Locate every leukocyte (white blood cell).
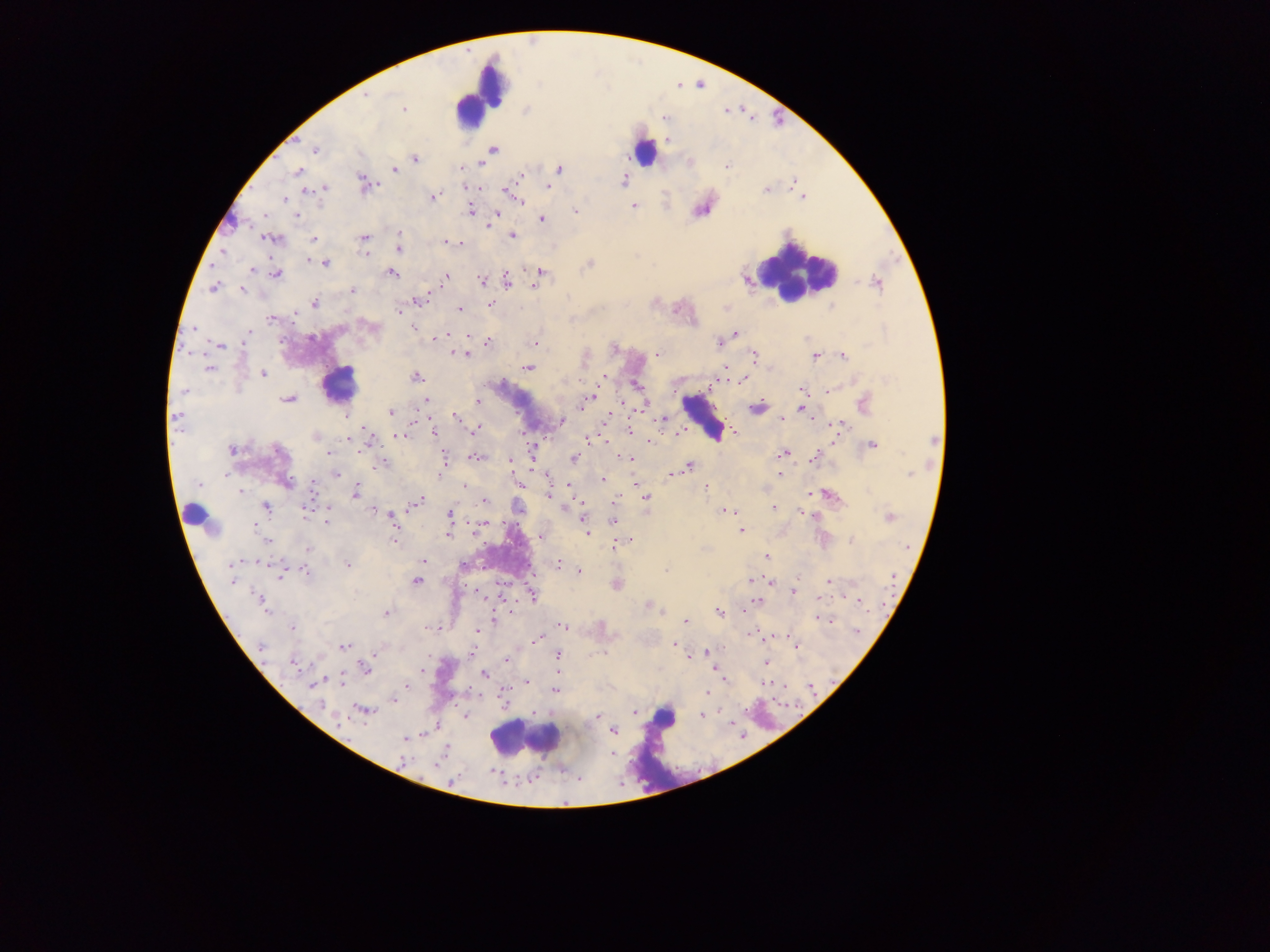
Approximate centers as (x, y) in pixels.
Leukocytes: (479, 94), (644, 152), (796, 272), (339, 383), (703, 418), (193, 516), (524, 739).

Summary:
  - Plasmodium parasite locations: (367, 96), (403, 110), (315, 149), (493, 150), (415, 159), (482, 163), (727, 165), (394, 169), (559, 169), (297, 171), (521, 176), (623, 180), (364, 183), (548, 187), (323, 188), (765, 190), (309, 191), (433, 197), (284, 200), (519, 201), (633, 207), (470, 210), (576, 210), (496, 215), (298, 216), (542, 220), (399, 233), (513, 236), (271, 239), (363, 239), (314, 240), (451, 243), (457, 243), (398, 248), (364, 253), (307, 260), (317, 261), (325, 263), (589, 264), (252, 270), (391, 273), (539, 273), (274, 275), (446, 277), (482, 281), (506, 281), (535, 284), (212, 287), (242, 290), (352, 290), (419, 300), (314, 303), (491, 305), (830, 307), (460, 309), (399, 310), (271, 319), (372, 327), (194, 328), (413, 329), (249, 333), (735, 333), (439, 338), (487, 342), (718, 342), (535, 344), (219, 346), (615, 348), (658, 354), (465, 355), (843, 355), (754, 356), (815, 356), (527, 368), (209, 369), (263, 373), (604, 376), (416, 377), (742, 381), (801, 390), (828, 390), (184, 391), (588, 398), (287, 399), (425, 401), (477, 402), (864, 404), (643, 409), (756, 409), (803, 409), (390, 413), (455, 415), (781, 418), (663, 419), (177, 420), (561, 421), (840, 425), (475, 429), (629, 430), (434, 432), (679, 432), (733, 432), (315, 436), (400, 436), (588, 439), (933, 441), (649, 442), (872, 445), (233, 450), (278, 451), (328, 453), (782, 453), (476, 456), (444, 458), (813, 458), (574, 459), (628, 459), (511, 460), (382, 465), (689, 466), (335, 474), (779, 474), (909, 474), (547, 475), (671, 475), (602, 479), (286, 482), (635, 482), (199, 484), (521, 485), (706, 486), (312, 487), (464, 487), (242, 492), (356, 492), (549, 495), (830, 496), (646, 498), (417, 501), (484, 501), (773, 507), (266, 508), (374, 510), (725, 510), (800, 511), (308, 513), (449, 516), (890, 516), (392, 518), (582, 519), (326, 520), (613, 520), (256, 525), (741, 531), (587, 533), (394, 534), (449, 535), (540, 536), (394, 540), (269, 541), (852, 541), (627, 544), (617, 545), (308, 549), (766, 557), (423, 561), (233, 564), (347, 564), (558, 564), (306, 571), (579, 571), (666, 571), (280, 573), (751, 579), (417, 581), (828, 581), (793, 592), (532, 595), (819, 598), (758, 600), (260, 601), (648, 605), (718, 612), (386, 613), (494, 619), (821, 619), (685, 621), (563, 626), (292, 627), (478, 631), (856, 632), (752, 634), (536, 639), (261, 645), (674, 645), (344, 647), (798, 647), (706, 652), (375, 654), (557, 655), (506, 659), (766, 663), (295, 665), (365, 668), (484, 675), (527, 681), (343, 682), (313, 684), (407, 686), (555, 690), (707, 692), (394, 700), (320, 705), (362, 710), (634, 712), (701, 715), (597, 716), (614, 730), (405, 738), (403, 761)
  - Capture: mobile-phone photograph through a microscope
  - Country: Ghana
  - Preparation: thick blood smear
  - Field of view: single
  - Image size: 1270×952 pixels